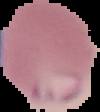
{
  "image_size": "100×112 pixels",
  "image_type": "cell region segmented out of the field of view; surrounding area masked to black",
  "result": "malaria parasites detected",
  "preparation": "thin blood smear"
}